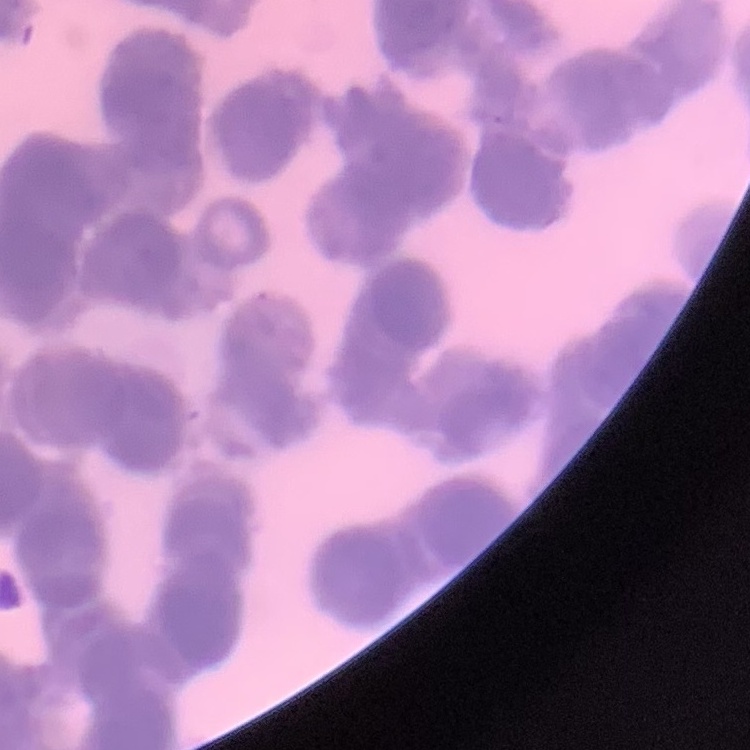

The red blood cells exhibit rouleaux formation. One tile cut from a larger photomicrograph. Field's or Giemsa stain. Thin peripheral smear.